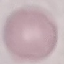

result = negative for malaria parasites
stain = Giemsa
preparation = thin blood smear
capture = smartphone through the microscope eyepiece
image type = cell patch, automatically extracted from a larger field of view and resized to 64 × 64 pixels